Assess this cell for malaria.
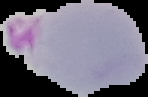
Parasitized.

{
  "preparation": "thin blood smear",
  "image_size": "148×97 pixels",
  "image_type": "segmented cell region on a black background"
}